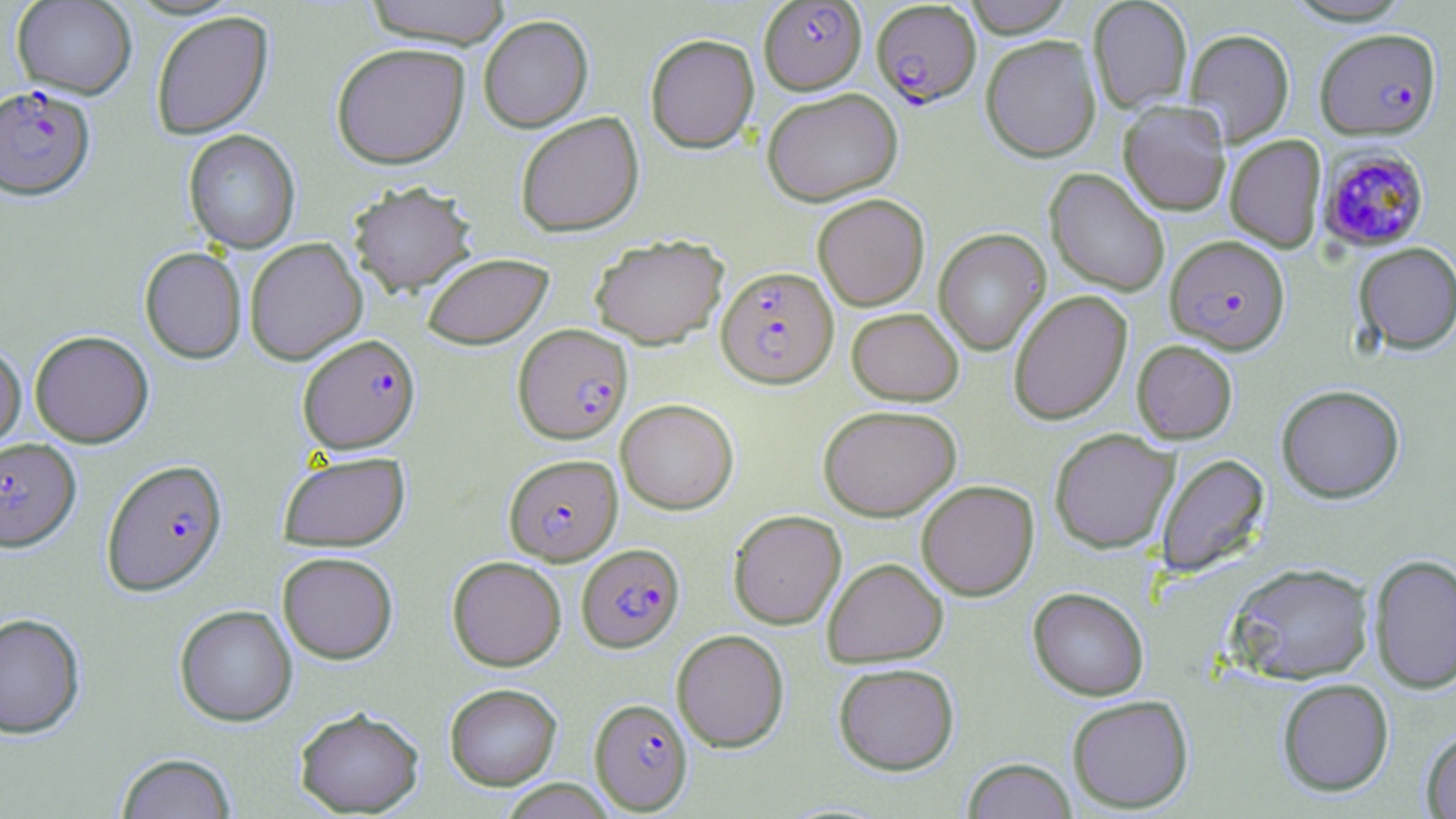
slide-level diagnosis = Plasmodium falciparum
modality = light microscopy
magnification = 1000x
preparation = thin blood film
image size = 1456×819 pixels
stain = May-Grünwald-Giemsa
Plasmodium falciparum-infected red blood cell locations = approximate bounding boxes as (x1, y1, x2, y2) in pixels: (758, 1, 866, 93), (871, 2, 981, 107), (1315, 28, 1441, 140), (0, 85, 95, 200), (1316, 147, 1430, 253), (1164, 234, 1291, 354), (716, 265, 839, 387), (513, 324, 633, 443), (298, 333, 420, 454), (0, 437, 81, 551), (504, 453, 622, 565), (101, 458, 228, 596), (577, 543, 684, 652), (589, 697, 693, 814)
uninfected red blood cell locations = approximate bounding boxes as (x1, y1, x2, y2) in pixels: (11, 0, 137, 98), (362, 0, 514, 47), (962, 0, 1075, 37), (1088, 0, 1192, 113), (1280, 0, 1417, 25), (150, 10, 274, 140), (478, 15, 594, 133), (1184, 28, 1294, 146), (645, 33, 759, 153), (980, 35, 1101, 162), (331, 42, 470, 169), (762, 87, 902, 206), (1118, 100, 1231, 216), (515, 112, 644, 237), (183, 129, 301, 253), (1225, 134, 1327, 253), (1045, 168, 1170, 296), (348, 181, 477, 296), (812, 194, 929, 310), (934, 229, 1050, 356), (590, 234, 729, 349), (244, 237, 367, 365), (1353, 242, 1456, 354), (139, 247, 247, 363), (422, 252, 554, 349), (1008, 290, 1132, 425), (846, 307, 963, 405), (29, 330, 154, 447), (1131, 340, 1238, 444), (0, 341, 26, 453), (1276, 384, 1405, 503), (616, 398, 739, 514), (818, 404, 961, 521), (1049, 428, 1179, 553), (278, 450, 410, 551), (1156, 453, 1270, 577), (916, 479, 1039, 600), (728, 509, 846, 629), (277, 551, 398, 663), (1368, 553, 1456, 695), (447, 555, 566, 671), (822, 557, 949, 668), (1227, 561, 1375, 685), (1027, 587, 1149, 701), (174, 604, 297, 726), (0, 612, 86, 739), (672, 629, 789, 752), (833, 662, 960, 775), (1277, 678, 1394, 797), (444, 683, 562, 789), (1066, 695, 1194, 813), (294, 706, 425, 817), (1421, 729, 1456, 818), (115, 752, 238, 818), (962, 758, 1077, 819), (498, 779, 618, 819)
field of view = single